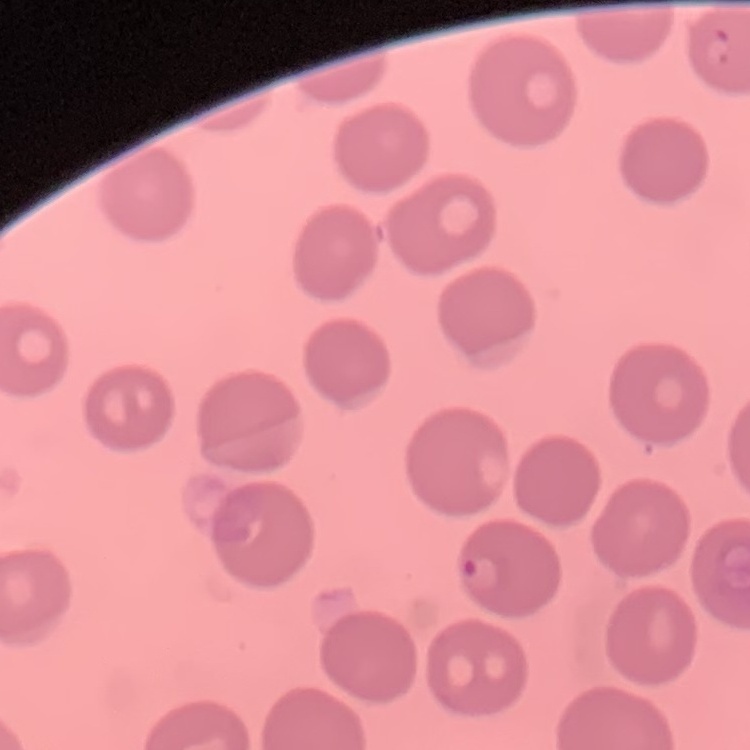

The erythrocytes show no rouleaux formation. Field's or Giemsa stain. One tile cut from a larger photomicrograph. Thin blood film.